Report the malaria status of this cell.
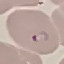

It is parasitized.

{
  "image_type": "cell patch, automatically extracted from a larger field of view and resized to 64 × 64 pixels",
  "stain": "Giemsa",
  "capture": "smartphone through the microscope eyepiece",
  "preparation": "thin smear"
}